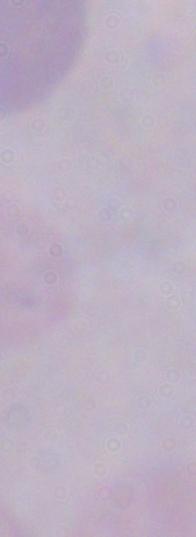
magnification = 1000x
modality = micrograph
identification = trypanosome